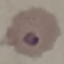 Malaria status: parasitized. Automatically extracted cell patch, resized to 64 × 64 pixels. Acquired by smartphone through the microscope eyepiece. Giemsa-stained preparation. Thin smear of blood.